Outline each blood parasite and name the species.
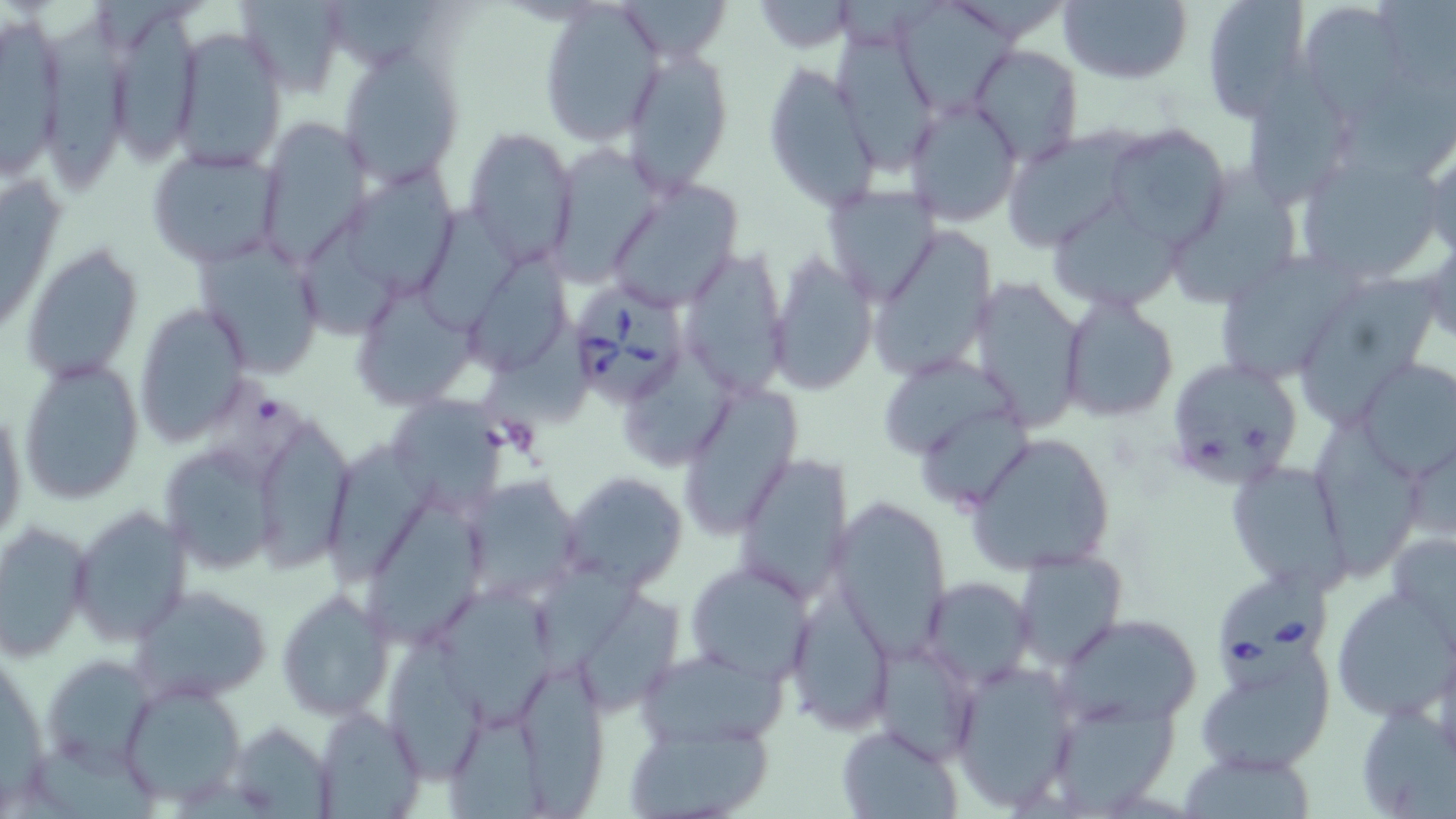

Approximate bounding boxes as (x1,y1)-(x2,y2) corner pairs in pixels.
Babesia divergens-infected red blood cells: (572,279)-(689,415), (1219,569)-(1327,699).
No Plasmodium falciparum, Plasmodium ovale, Plasmodium malariae, Plasmodium vivax, or Trypanosoma brucei observed.

Summary:
  - Uninfected red blood cell locations: (236,0)-(349,98), (1058,0)-(1192,85), (1200,0)-(1309,120), (1300,1)-(1411,115), (751,2)-(857,53), (538,3)-(666,146), (1,9)-(70,180), (117,9)-(199,168), (48,10)-(125,195), (170,26)-(288,169), (969,43)-(1082,167), (339,47)-(465,188), (618,47)-(734,194), (761,64)-(882,213), (903,97)-(1022,226), (253,116)-(373,271), (1103,124)-(1233,250), (463,128)-(578,266), (1000,128)-(1140,252), (1251,128)-(1352,218), (1420,140)-(1455,262), (546,143)-(664,284), (146,146)-(287,268), (1297,158)-(1449,285), (1,165)-(66,344), (351,165)-(460,298), (1175,166)-(1302,307), (605,177)-(743,309), (821,184)-(941,307), (1053,200)-(1184,306), (421,202)-(521,336), (302,213)-(400,344), (870,228)-(999,385), (1425,236)-(1455,349), (195,239)-(327,378), (22,242)-(143,386), (681,247)-(789,397), (767,252)-(878,394), (1220,255)-(1365,383), (469,256)-(575,375), (968,276)-(1087,429), (1298,279)-(1441,432), (358,289)-(483,416), (1058,296)-(1179,423), (134,304)-(250,446), (477,317)-(592,437), (619,345)-(741,467), (1164,357)-(1303,489), (19,358)-(144,505), (887,359)-(1022,457), (1354,361)-(1455,479), (676,383)-(804,537), (381,389)-(515,515), (0,396)-(27,557), (1315,408)-(1424,584), (922,409)-(1028,514), (258,412)-(361,577), (967,430)-(1117,573), (1405,440)-(1456,545), (328,443)-(446,592), (162,447)-(276,581), (732,453)-(854,603), (1226,461)-(1348,593), (564,468)-(688,590), (471,476)-(575,598), (366,499)-(487,653), (831,499)-(953,660), (68,503)-(192,646), (0,521)-(95,661), (1385,529)-(1456,646), (1011,550)-(1127,671), (685,560)-(817,684), (533,567)-(645,691), (922,578)-(1034,687), (131,583)-(272,705), (789,586)-(894,729), (436,587)-(555,731), (1331,587)-(1456,720), (277,589)-(393,721), (582,592)-(691,720), (1060,614)-(1201,725), (388,632)-(483,785), (869,638)-(982,764), (1197,643)-(1334,774), (637,647)-(789,750), (43,653)-(159,775), (948,659)-(1080,809), (519,664)-(611,819), (120,682)-(247,806), (1052,702)-(1184,819), (1357,702)-(1455,818), (314,706)-(428,816), (448,720)-(549,819), (626,720)-(774,817), (228,722)-(333,816), (836,723)-(963,818), (33,737)-(160,819), (1182,765)-(1322,819)
  - Slide-level diagnosis: Babesia divergens
  - Image size: 1456×819 pixels
  - Modality: light microscopy
  - Magnification: 1000x
  - Preparation: thin blood smear
  - Stain: May-Grünwald-Giemsa
  - Field of view: single